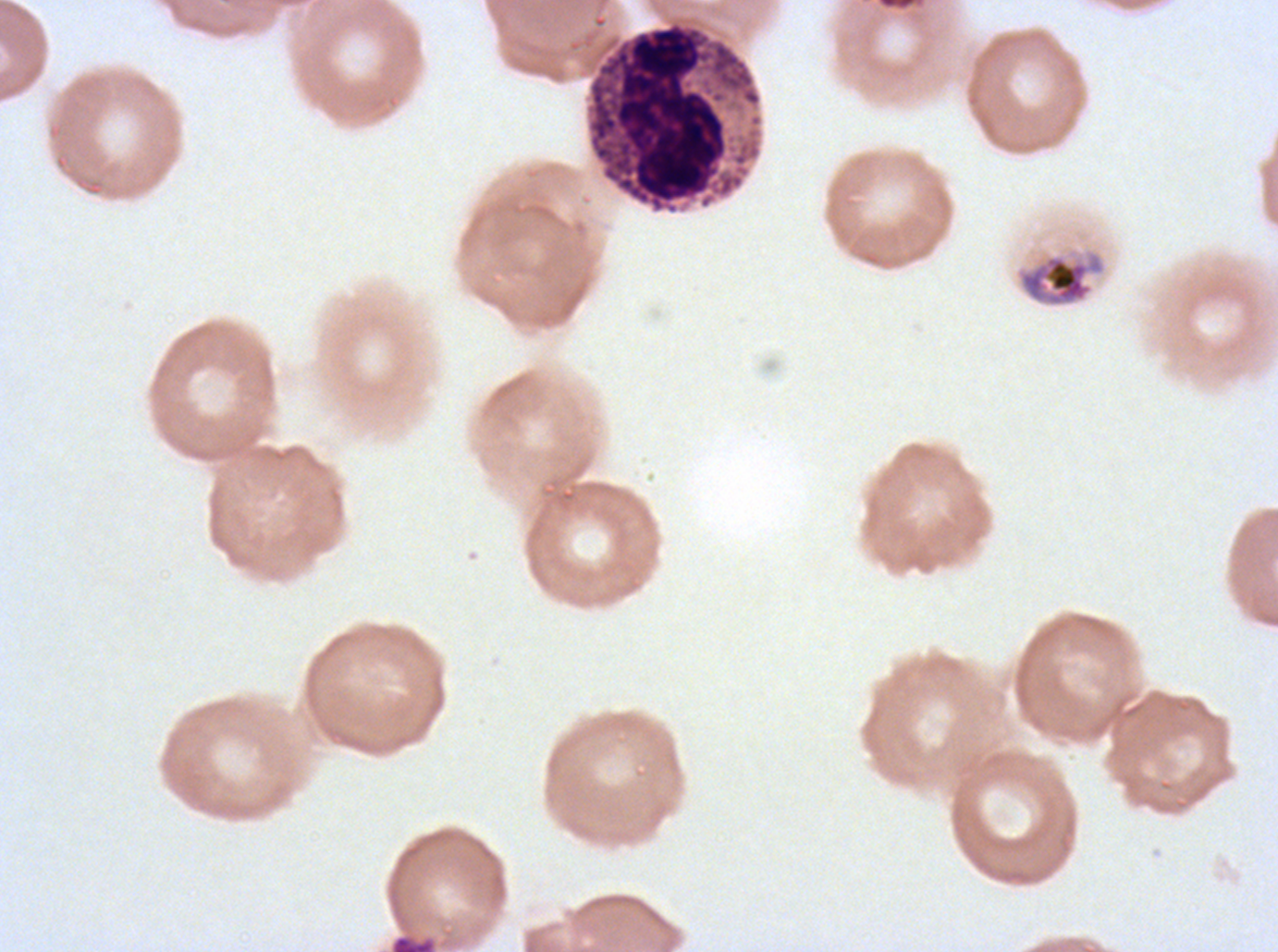

notation = approximate bounding boxes as {x1, y1, x2, y2} in pixels
mid trophozoite locations = {1014, 245, 1109, 309}
late schizont locations = {390, 934, 436, 951}
leukocyte locations = {584, 15, 764, 216}
stain = Giemsa
preparation = thin blood film
image size = 1278×952 pixels
life-cycle stages observed = mid trophozoite, late schizont
specimen = ex-vivo P. falciparum culture from a patient in The Gambia, grown for 24 to 48 hours
field of view = one sub-image of a larger composite